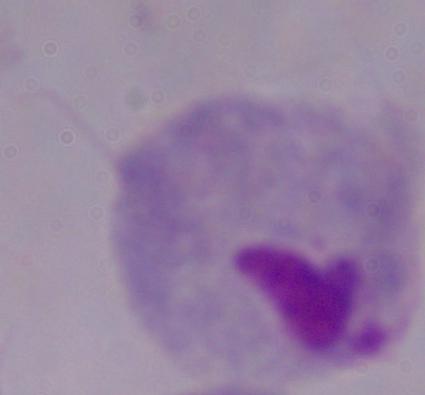
A trichomonad is shown. 1000x magnification. Photomicrograph.